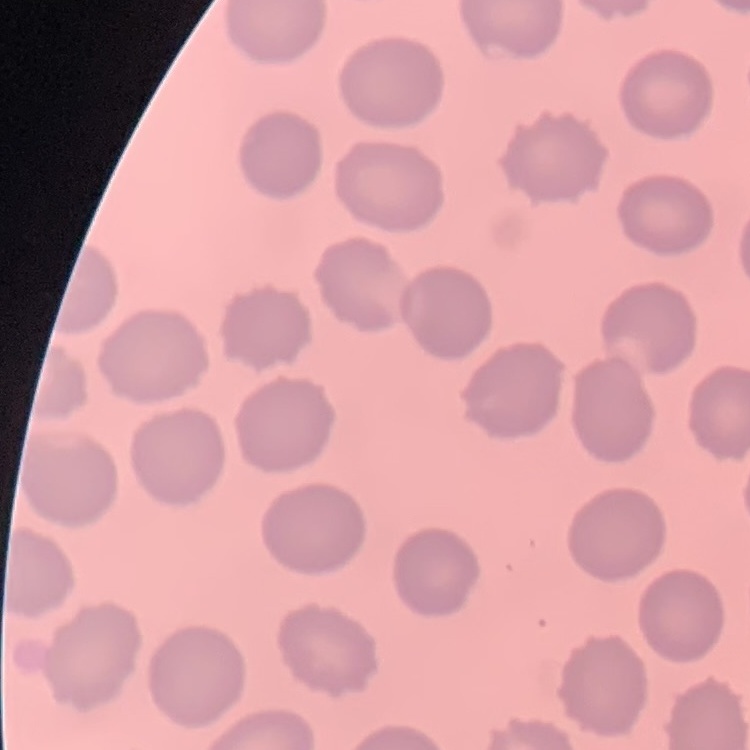
red_blood_cell_morphology: no rouleaux formation
stain: Field's or Giemsa
preparation: thin peripheral smear
image_type: one tile cut from a larger photomicrograph